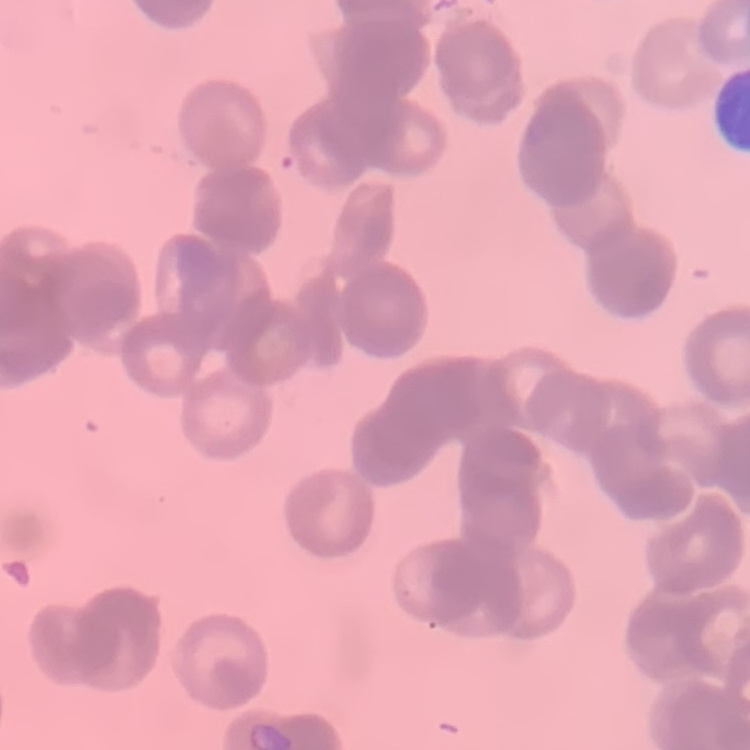

The erythrocytes exhibit rouleaux formation. Stained with either Field's or Giemsa. Thin peripheral smear. Square crop of a larger photomicrograph.